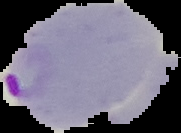
From a thin blood film. Result: Plasmodium parasites identified. Image is 181×133 pixels. Segmented cell region on a black background.